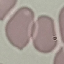

result = no malaria parasites detected
capture = smartphone camera at the microscope eyepiece
image type = cell patch, automatically extracted from a larger field of view and resized to 64 × 64 pixels
preparation = thin blood smear
stain = Giemsa